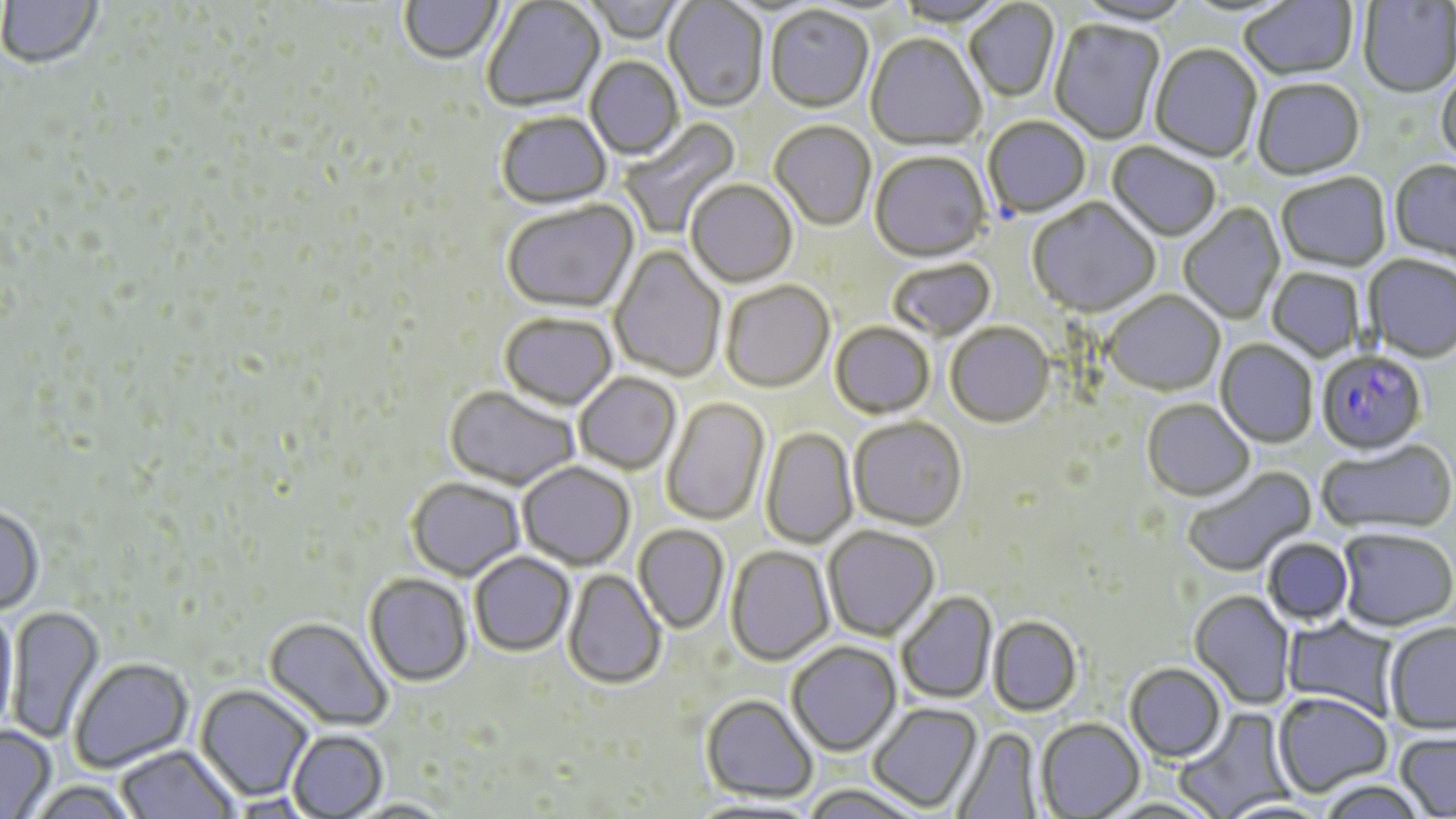

Plasmodium falciparum-infected red blood cell locations = approximate bounding boxes as [x1, y1, x2, y2] in pixels: [1316, 353, 1427, 458]
slide-level diagnosis = Plasmodium falciparum
uninfected red blood cell locations = approximate bounding boxes as [x1, y1, x2, y2] in pixels: [0, 0, 103, 69], [1240, 0, 1358, 82], [399, 1, 504, 68], [482, 1, 606, 115], [582, 1, 687, 45], [664, 1, 768, 114], [893, 1, 1011, 29], [964, 1, 1061, 103], [1072, 1, 1195, 29], [1358, 2, 1456, 100], [765, 7, 873, 115], [1049, 20, 1165, 145], [865, 35, 986, 153], [1150, 45, 1262, 164], [585, 57, 684, 160], [1436, 70, 1456, 172], [1253, 81, 1365, 182], [496, 113, 612, 212], [619, 117, 742, 240], [983, 117, 1091, 219], [770, 122, 876, 232], [1106, 143, 1220, 244], [870, 153, 990, 264], [1389, 161, 1456, 269], [1276, 174, 1391, 274], [685, 181, 798, 289], [1028, 199, 1161, 320], [502, 200, 640, 315], [1179, 204, 1286, 325], [608, 245, 726, 382], [1363, 256, 1456, 365], [888, 259, 997, 343], [1266, 268, 1365, 362], [720, 282, 834, 393], [1102, 292, 1225, 397], [499, 314, 618, 411], [945, 323, 1055, 429], [830, 324, 935, 419], [1216, 340, 1318, 449], [573, 372, 681, 474], [444, 385, 581, 490], [661, 397, 770, 526], [1142, 401, 1255, 502], [848, 417, 967, 531], [761, 427, 858, 549], [1317, 440, 1456, 538], [517, 461, 635, 570], [1182, 465, 1317, 577], [407, 477, 525, 580], [0, 504, 44, 615], [634, 524, 729, 634], [823, 525, 939, 641], [1337, 528, 1455, 633], [1262, 537, 1355, 627], [725, 545, 834, 667], [470, 551, 575, 656], [563, 569, 665, 690], [364, 573, 473, 687], [1189, 590, 1296, 710], [896, 591, 998, 705], [6, 604, 104, 743], [0, 609, 19, 736], [988, 615, 1082, 716], [263, 616, 392, 731], [1282, 617, 1400, 720], [1384, 622, 1456, 735], [787, 640, 902, 756], [68, 656, 194, 773], [1124, 663, 1227, 764], [195, 684, 313, 802], [1273, 692, 1393, 798], [701, 694, 817, 802], [867, 702, 982, 812], [1174, 706, 1295, 818], [1036, 718, 1144, 817], [0, 724, 56, 818], [951, 727, 1043, 819], [287, 729, 388, 818], [1394, 730, 1456, 818], [116, 744, 238, 818], [1314, 779, 1433, 818], [25, 780, 142, 819], [800, 785, 926, 819], [228, 793, 317, 818], [346, 799, 458, 818]
field of view = single
stain = May-Grünwald-Giemsa
preparation = thin blood film
modality = optical microscopy
image size = 1456×819 pixels
magnification = 1000x